Outline each Plasmodium ovale-infected red blood cell.
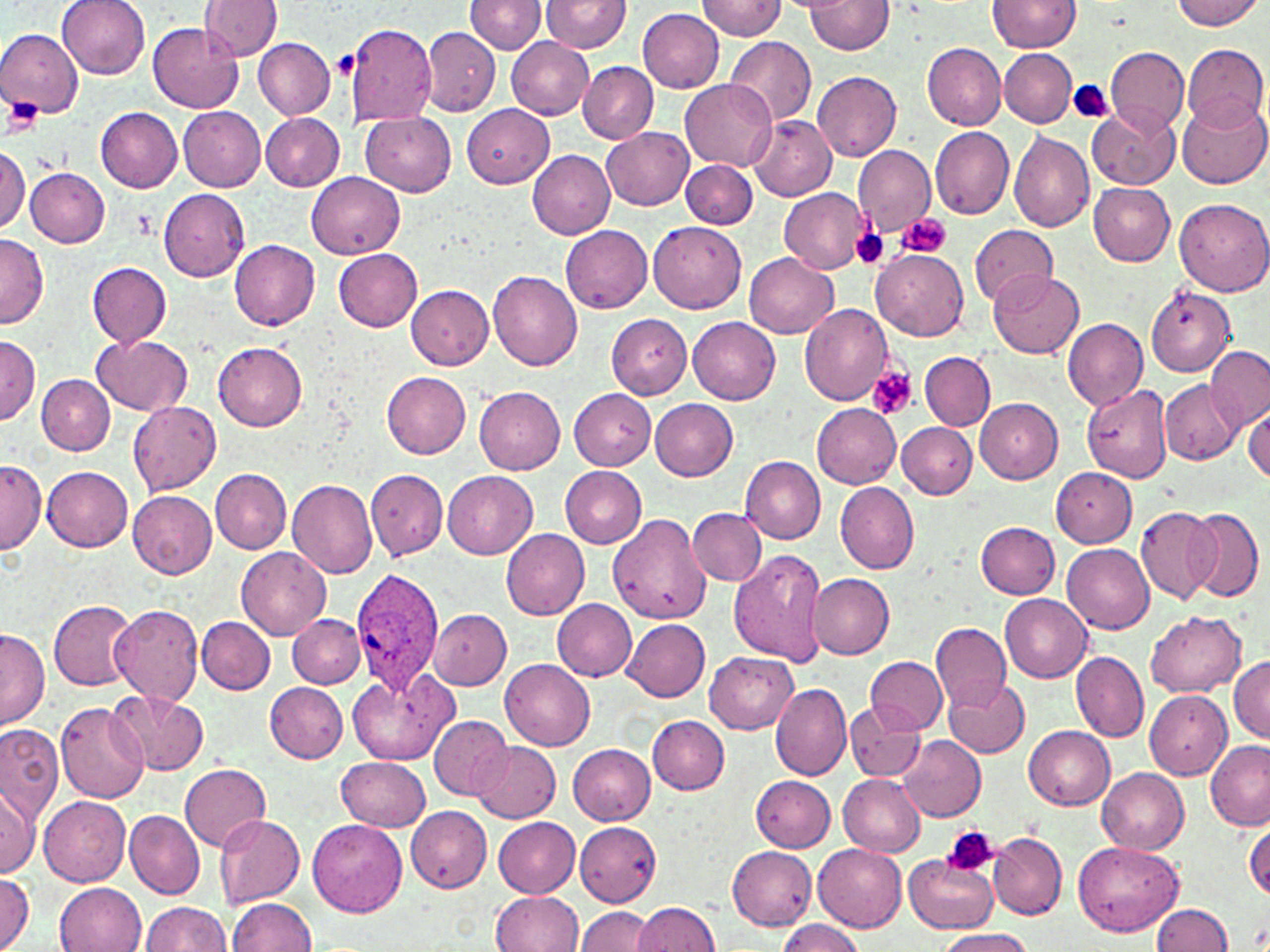

Approximate bounding boxes as (x1, y1, x2, y2) in pixels.
Plasmodium ovale-infected red blood cells: (351, 568, 443, 692).

slide_level_diagnosis: Plasmodium ovale
preparation: thin blood smear
platelet_locations: 'approximate bounding boxes as (x1, y1, x2, y2) in pixels: (331, 51, 358, 80), (1070, 80, 1114, 125), (5, 96, 40, 135), (129, 208, 156, 241), (896, 213, 952, 259), (849, 226, 890, 270), (867, 366, 917, 420), (941, 825, 997, 877)'
uninfected_red_blood_cell_locations: 'approximate bounding boxes as (x1, y1, x2, y2) in pixels: (58, 0, 150, 79), (465, 0, 545, 53), (541, 0, 631, 53), (693, 0, 783, 40), (992, 0, 1082, 52), (1170, 0, 1264, 30), (199, 1, 282, 60), (806, 1, 894, 53), (637, 7, 724, 94), (344, 22, 438, 127), (148, 23, 244, 114), (421, 25, 499, 116), (1, 28, 82, 118), (252, 36, 335, 119), (505, 36, 593, 119), (724, 36, 816, 128), (1182, 43, 1267, 131), (923, 44, 1006, 129), (1105, 47, 1190, 135), (999, 48, 1077, 127), (577, 60, 658, 143), (813, 71, 901, 162), (679, 80, 776, 170), (1178, 97, 1269, 189), (463, 103, 553, 189), (95, 106, 184, 192), (179, 106, 266, 193), (1088, 106, 1179, 189), (261, 112, 345, 191), (360, 112, 457, 196), (749, 117, 837, 201), (930, 125, 1014, 217), (600, 126, 694, 210), (1009, 132, 1095, 232), (0, 145, 28, 234), (853, 145, 935, 234), (528, 150, 616, 240), (681, 160, 758, 229), (24, 167, 110, 246), (307, 172, 404, 258), (1088, 183, 1175, 265), (156, 187, 250, 280), (779, 187, 870, 274), (1173, 198, 1270, 296), (649, 221, 746, 314), (971, 223, 1058, 307), (560, 224, 654, 311), (0, 232, 48, 327), (229, 239, 321, 329), (870, 248, 968, 341), (334, 249, 422, 331), (743, 252, 839, 338), (88, 262, 171, 348), (489, 270, 583, 371), (988, 271, 1084, 360), (406, 285, 493, 369), (1146, 289, 1232, 376), (799, 304, 893, 405), (604, 312, 692, 400), (688, 316, 780, 405), (1063, 319, 1147, 410), (93, 335, 192, 416), (0, 336, 39, 425), (213, 343, 307, 430), (1203, 346, 1270, 430), (920, 352, 996, 429), (381, 372, 470, 459), (37, 374, 114, 454), (1159, 380, 1241, 465), (1082, 383, 1172, 484), (474, 385, 565, 475), (569, 389, 656, 469), (975, 397, 1064, 483), (649, 398, 738, 481), (128, 401, 222, 495), (812, 404, 902, 488), (1245, 406, 1270, 486), (896, 422, 976, 499), (740, 456, 827, 544), (0, 459, 45, 553), (559, 465, 647, 548), (42, 466, 133, 551), (1050, 468, 1137, 547), (211, 469, 291, 554), (366, 469, 448, 561), (442, 469, 538, 559), (286, 478, 378, 579), (836, 483, 920, 573), (126, 489, 218, 579), (1135, 507, 1222, 604), (687, 508, 766, 585), (1185, 508, 1264, 603), (612, 513, 708, 621), (976, 521, 1060, 600), (501, 528, 590, 619), (1063, 544, 1154, 633), (235, 546, 331, 639), (729, 550, 828, 667), (807, 571, 895, 658), (1000, 594, 1093, 683), (552, 599, 637, 681), (49, 600, 141, 690), (110, 603, 204, 707), (428, 607, 512, 689), (1146, 611, 1246, 698), (288, 614, 367, 688), (195, 616, 275, 694), (622, 618, 710, 702), (931, 623, 1011, 710), (0, 628, 49, 730), (704, 651, 798, 734), (1071, 651, 1149, 743), (860, 654, 955, 805), (866, 657, 947, 734), (1229, 657, 1270, 743), (501, 659, 595, 749), (347, 670, 458, 765), (942, 678, 1031, 758), (265, 683, 348, 763), (771, 683, 852, 781), (1144, 690, 1232, 780), (110, 691, 210, 776), (55, 700, 149, 804), (844, 702, 924, 782), (647, 715, 729, 794), (430, 716, 512, 800), (0, 724, 64, 823), (1024, 725, 1115, 810), (899, 735, 986, 821), (1204, 740, 1270, 830), (472, 741, 561, 823), (568, 743, 655, 826), (336, 756, 431, 830), (179, 763, 271, 850), (1098, 767, 1190, 856), (750, 775, 835, 852), (838, 775, 926, 856), (0, 784, 38, 878), (39, 795, 132, 886), (407, 806, 492, 893), (125, 808, 205, 899), (215, 814, 305, 908), (492, 816, 581, 896), (308, 818, 407, 918), (1245, 822, 1270, 903), (574, 823, 659, 905), (987, 831, 1066, 922), (1074, 841, 1183, 936), (814, 843, 908, 929), (726, 846, 818, 930), (905, 854, 997, 932), (1, 868, 33, 952), (54, 881, 148, 952), (490, 891, 584, 951), (227, 898, 318, 951), (140, 900, 230, 952), (632, 901, 720, 951), (1152, 904, 1234, 951), (576, 906, 654, 952), (776, 919, 864, 952), (937, 927, 1036, 952)'
magnification: 1000x
image_size: 1270×952 pixels
field_of_view: one of a larger specimen
stain: May-Grünwald-Giemsa
modality: light microscopy